Assess the morphology of the red blood cells.
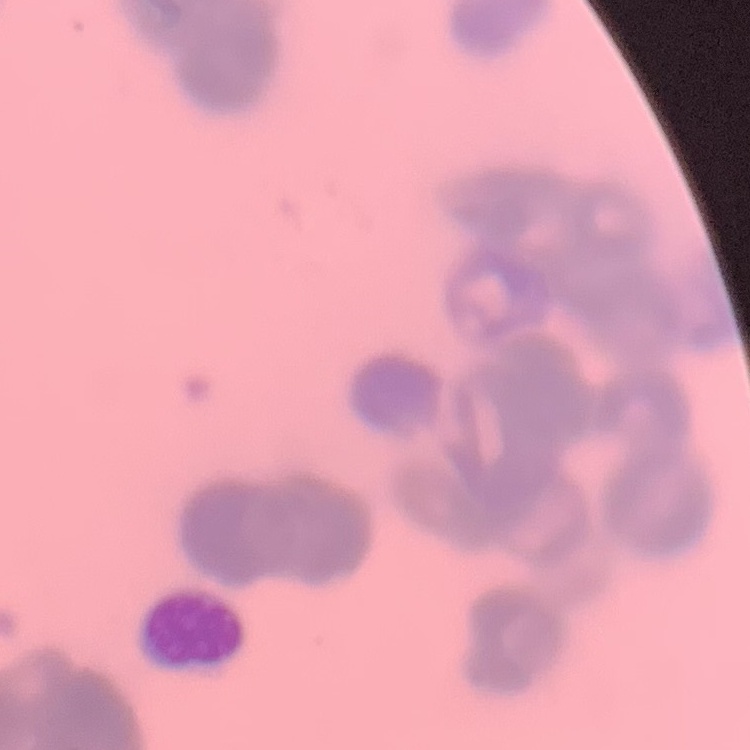
Rouleaux formation.

Summary:
  - Stain: Field's or Giemsa
  - Image type: square crop of a larger photomicrograph
  - Preparation: thin peripheral smear